Comment on the morphology of the erythrocytes.
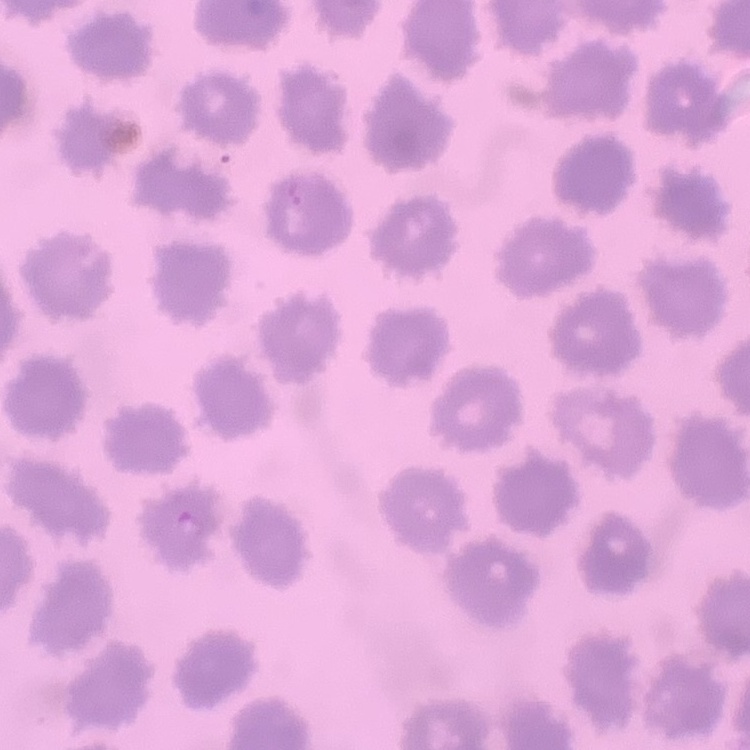

They show no rouleaux formation.

Summary:
  - Stain: Field's or Giemsa
  - Image type: one tile cut from a larger photomicrograph
  - Preparation: thin blood film